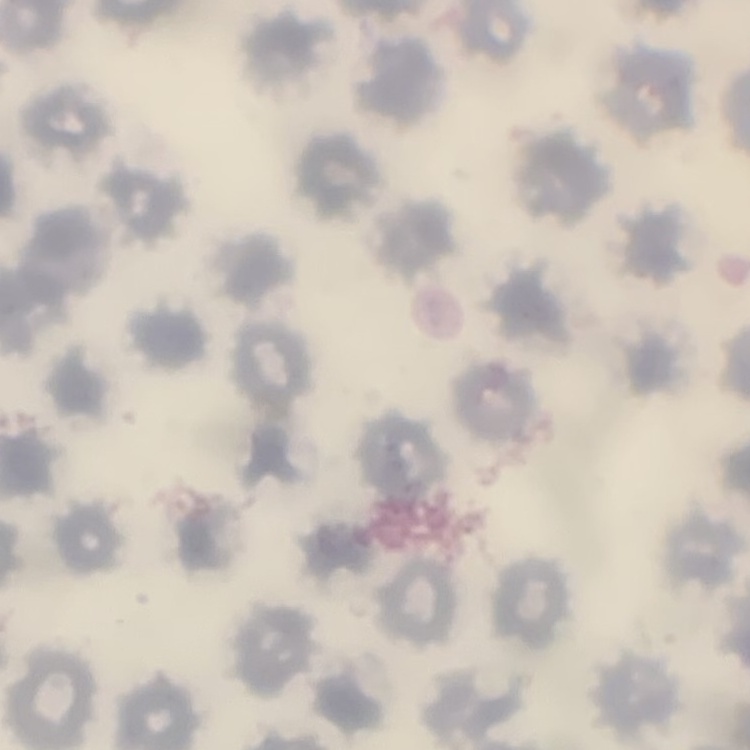

The red blood cells show no rouleaux formation. Stained with either Field's or Giemsa. Thin peripheral smear. One tile cut from a larger photomicrograph.